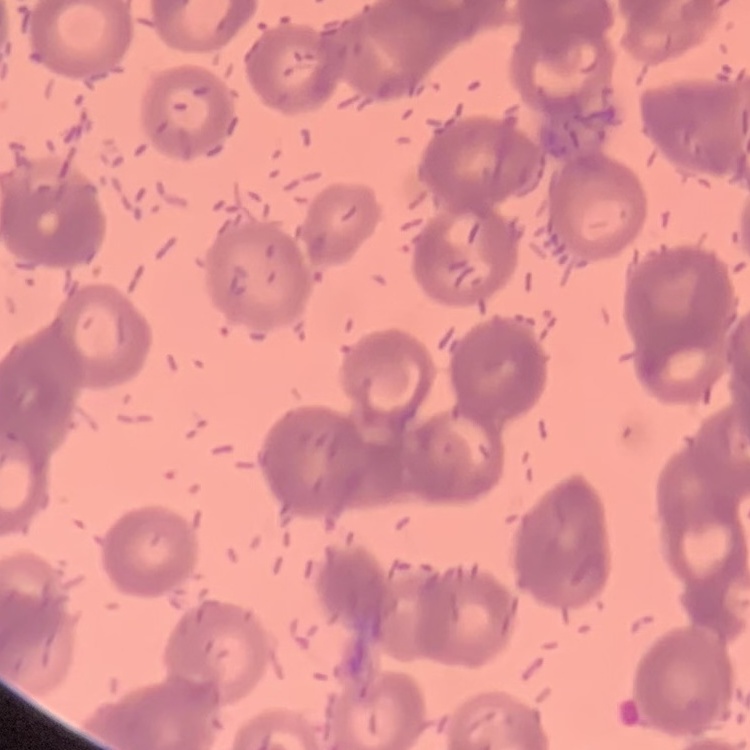 The erythrocytes show rouleaux formation. Thin peripheral smear. Square crop of a larger photomicrograph. Field's or Giemsa stain.